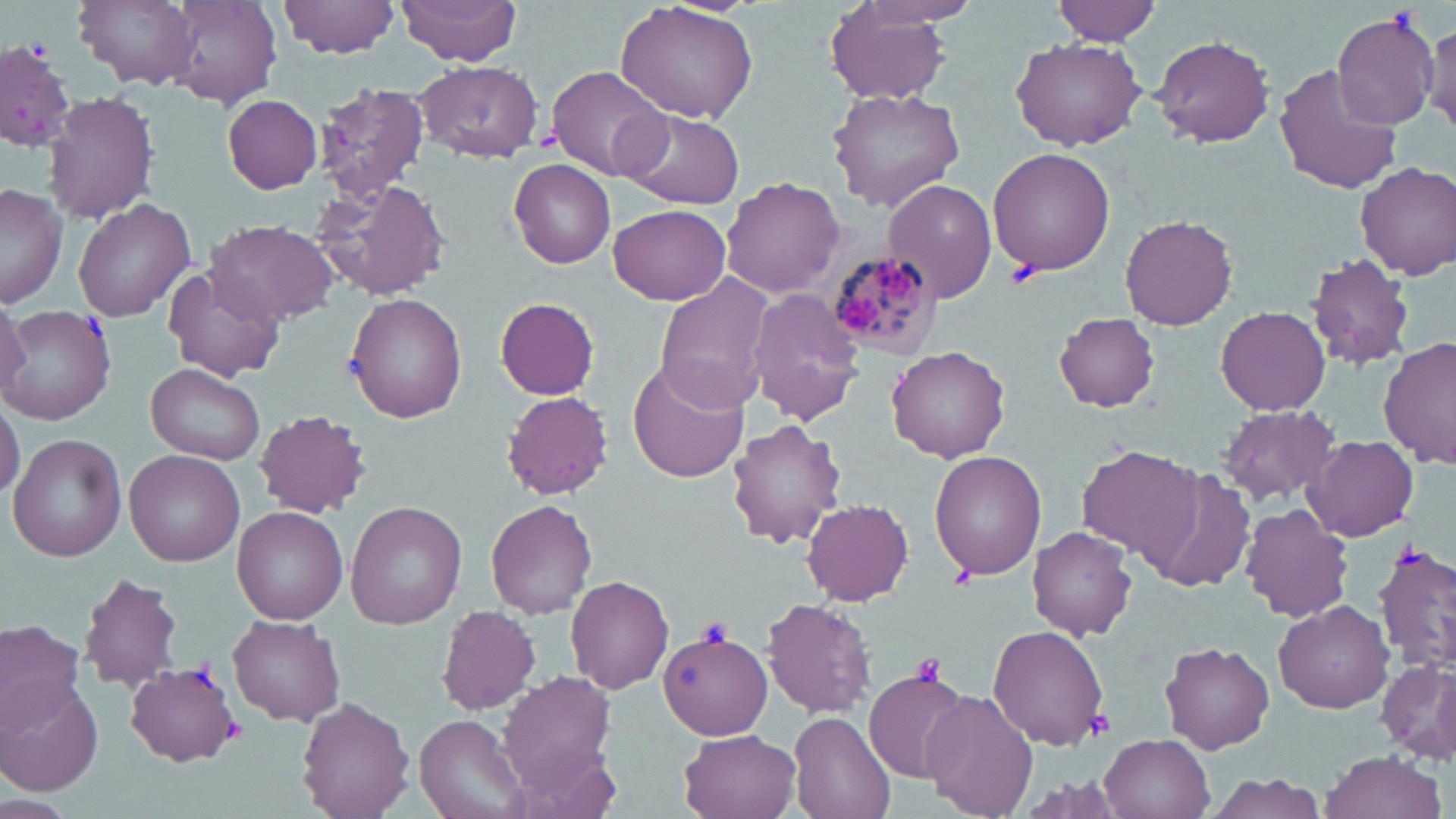

{
  "slide_level_diagnosis": "Plasmodium malariae",
  "platelet_locations": "approximate bounding boxes as (x1,y1)-(x2,y2) corner pairs in pixels: (1006,256)-(1042,287), (698,618)-(733,647), (910,653)-(950,685), (1083,709)-(1114,740)",
  "stain": "May-Grünwald-Giemsa",
  "modality": "light microscopy",
  "field_of_view": "single",
  "magnification": "1000x",
  "plasmodium_malariae_infected_red_blood_cell_locations": "approximate bounding boxes as (x1,y1)-(x2,y2) corner pairs in pixels: (826,250)-(941,361)",
  "uninfected_red_blood_cell_locations": "approximate bounding boxes as (x1,y1)-(x2,y2) corner pairs in pixels: (75,0)-(198,88), (167,0)-(282,108), (279,0)-(401,57), (397,0)-(522,65), (1053,0)-(1163,45), (614,1)-(759,123), (824,4)-(955,105), (1329,9)-(1441,131), (1424,17)-(1456,136), (1151,35)-(1276,147), (1012,37)-(1146,150), (0,42)-(77,150), (1,42)-(72,154), (417,62)-(542,161), (1275,63)-(1401,194), (548,66)-(675,182), (313,82)-(430,203), (829,88)-(965,211), (43,92)-(159,224), (223,95)-(321,193), (623,109)-(744,209), (987,147)-(1114,275), (509,160)-(616,269), (1357,161)-(1456,278), (319,178)-(450,302), (721,178)-(846,297), (882,178)-(997,302), (0,184)-(66,307), (73,197)-(196,321), (608,203)-(730,306), (1119,215)-(1239,329), (206,219)-(339,327), (1306,254)-(1416,371), (162,266)-(286,383), (654,275)-(774,414), (747,286)-(870,425), (345,294)-(467,424), (496,297)-(599,399), (0,298)-(32,396), (3,306)-(116,424), (1217,306)-(1329,416), (1053,312)-(1161,411), (1377,337)-(1454,471), (886,347)-(1011,462), (628,359)-(750,484), (147,363)-(265,464), (502,391)-(614,499), (0,397)-(24,502), (1217,403)-(1345,508), (255,410)-(370,517), (727,418)-(845,548), (8,433)-(127,561), (1305,435)-(1418,542), (1077,446)-(1205,566), (125,450)-(245,567), (929,451)-(1047,580), (1138,470)-(1257,589), (486,498)-(598,618), (346,500)-(467,627), (802,500)-(914,604), (1241,505)-(1353,622), (232,507)-(347,623), (1028,526)-(1136,640), (1375,547)-(1456,671), (79,574)-(184,691), (565,575)-(673,693), (764,596)-(876,719), (1273,599)-(1393,712), (436,605)-(542,714), (228,614)-(345,726), (0,619)-(87,734), (987,625)-(1109,751), (659,630)-(772,739), (1158,642)-(1275,755), (1378,655)-(1455,763), (127,662)-(241,766), (865,668)-(971,784), (498,670)-(618,791), (2,681)-(103,798), (922,689)-(1039,818), (298,696)-(414,818), (788,713)-(895,819), (417,715)-(525,819), (678,729)-(801,819), (1102,734)-(1214,819), (1319,751)-(1447,819)",
  "preparation": "thin blood film",
  "image_size": "1456×819 pixels"
}